Report the malaria status of this cell.
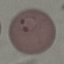

Parasitized.

preparation: thin blood smear
capture: smartphone through the microscope eyepiece
stain: Giemsa
image_type: automatically extracted cell patch, resized to 64 × 64 pixels